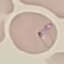

{
  "result": "malaria parasites detected",
  "image_type": "automatically extracted cell patch, resized to 64 × 64 pixels",
  "preparation": "thin blood smear",
  "capture": "smartphone through the microscope eyepiece",
  "stain": "Giemsa"
}